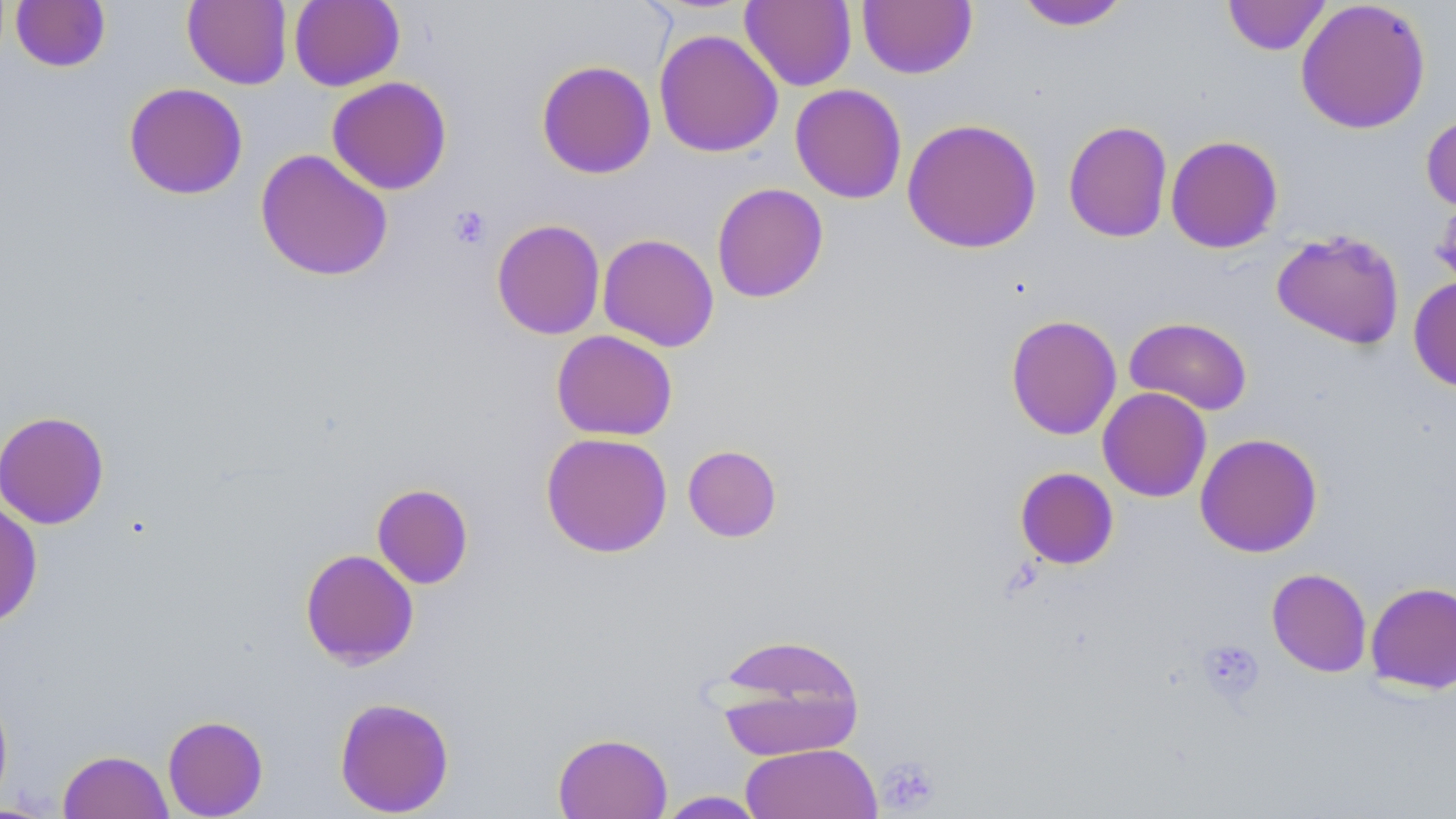 Approximate bounding boxes as named x1/y1/x2/y2 corners in pixels. Platelet locations: (x1=448, y1=205, x2=491, y2=249), (x1=1197, y1=638, x2=1265, y2=703), (x1=876, y1=754, x2=942, y2=814). Uninfected red blood cell locations: (x1=10, y1=0, x2=111, y2=73), (x1=182, y1=0, x2=292, y2=89), (x1=289, y1=0, x2=405, y2=91), (x1=1223, y1=0, x2=1331, y2=56), (x1=1295, y1=0, x2=1432, y2=135), (x1=740, y1=1, x2=856, y2=91), (x1=857, y1=1, x2=977, y2=79), (x1=1014, y1=1, x2=1132, y2=32), (x1=653, y1=29, x2=783, y2=158), (x1=536, y1=59, x2=657, y2=179), (x1=326, y1=76, x2=453, y2=195), (x1=123, y1=82, x2=248, y2=200), (x1=789, y1=83, x2=907, y2=203), (x1=1421, y1=112, x2=1456, y2=214), (x1=901, y1=118, x2=1042, y2=254), (x1=1063, y1=120, x2=1173, y2=243), (x1=1165, y1=135, x2=1283, y2=253), (x1=255, y1=149, x2=393, y2=282), (x1=711, y1=182, x2=829, y2=303), (x1=1432, y1=194, x2=1456, y2=292), (x1=491, y1=218, x2=605, y2=340), (x1=1272, y1=230, x2=1406, y2=350), (x1=597, y1=233, x2=720, y2=352), (x1=1408, y1=276, x2=1456, y2=392), (x1=1005, y1=314, x2=1122, y2=440), (x1=1124, y1=317, x2=1253, y2=415), (x1=551, y1=330, x2=678, y2=441), (x1=1097, y1=387, x2=1212, y2=502), (x1=0, y1=410, x2=110, y2=529), (x1=540, y1=432, x2=673, y2=558), (x1=1195, y1=432, x2=1323, y2=558), (x1=682, y1=444, x2=782, y2=542), (x1=1014, y1=467, x2=1119, y2=570), (x1=371, y1=484, x2=474, y2=589), (x1=0, y1=500, x2=43, y2=628), (x1=300, y1=549, x2=419, y2=669), (x1=1266, y1=568, x2=1372, y2=676), (x1=1365, y1=582, x2=1456, y2=694), (x1=709, y1=633, x2=866, y2=761), (x1=0, y1=686, x2=13, y2=813), (x1=334, y1=697, x2=455, y2=816), (x1=162, y1=715, x2=268, y2=818), (x1=552, y1=732, x2=673, y2=819), (x1=741, y1=742, x2=882, y2=819), (x1=58, y1=750, x2=173, y2=819), (x1=655, y1=791, x2=769, y2=818). Slide-level diagnosis: no evidence of blood parasites. Optical microscopy. Image is 1456×819 pixels. Thin blood smear. One field of a larger specimen. 1000x magnification. May-Grünwald-Giemsa stain.